Comment on the morphology of the erythrocytes.
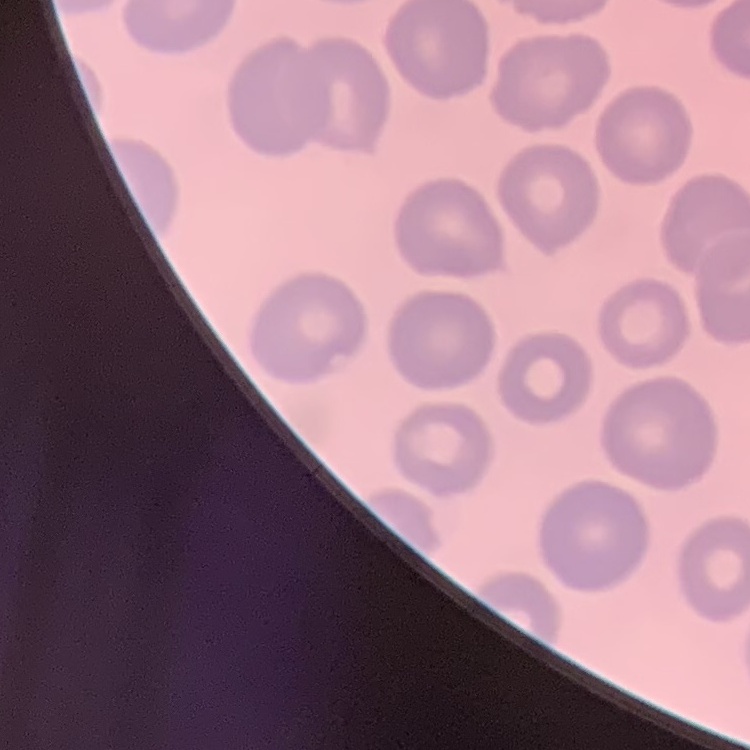
They show no rouleaux formation.

image_type: one tile cut from a larger photomicrograph
preparation: thin blood smear
stain: Field's or Giemsa